Locate and identify every blood parasite.
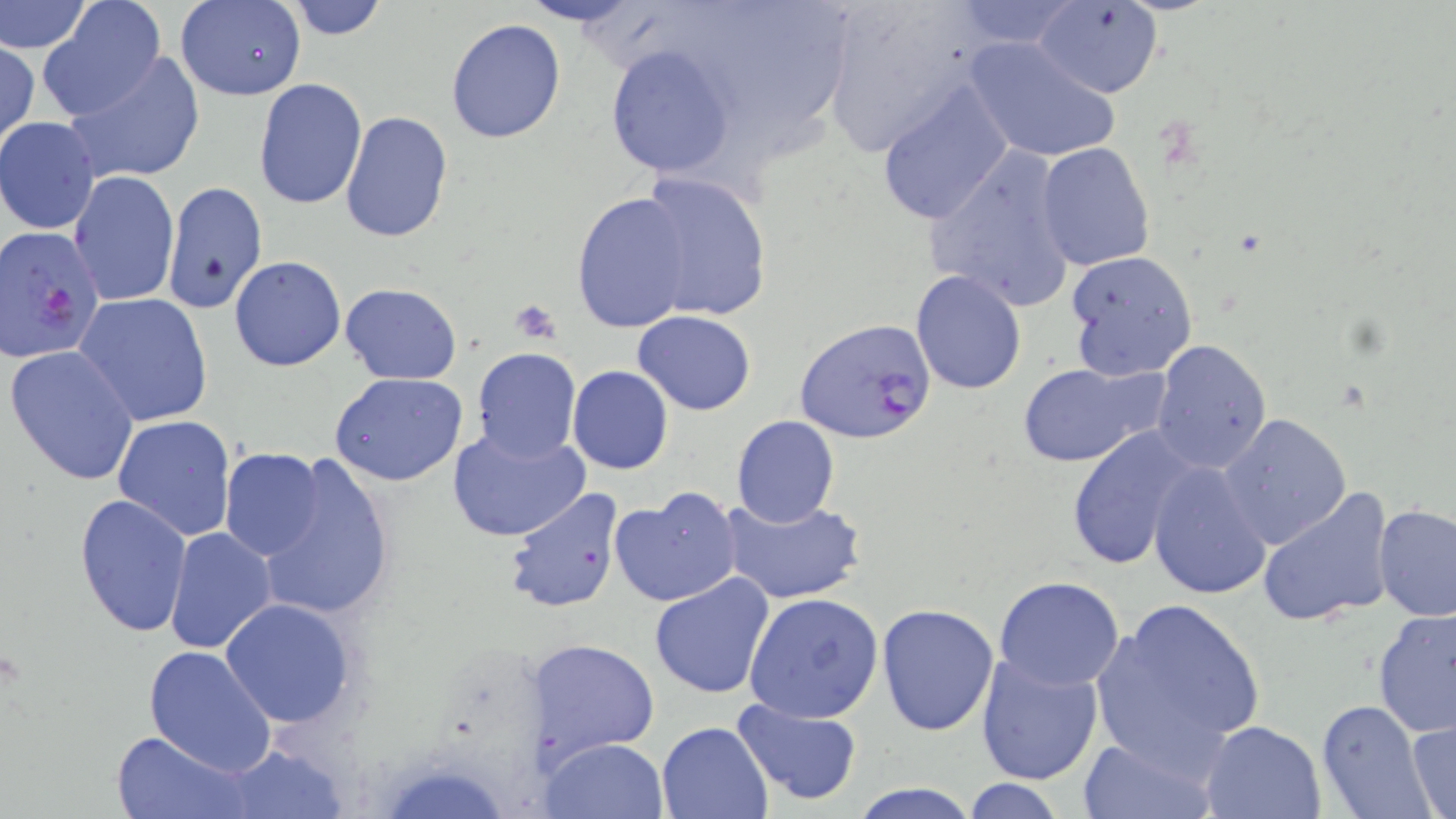
Approximate bounding boxes as named x1/y1/x2/y2 corners in pixels.
Plasmodium falciparum-infected red blood cells: (x1=1, y1=225, x2=105, y2=363), (x1=795, y1=319, x2=939, y2=446).
No Plasmodium ovale, Plasmodium malariae, Plasmodium vivax, Babesia divergens, or Trypanosoma brucei observed.

Platelet locations: (x1=507, y1=298, x2=561, y2=343). Uninfected red blood cell locations: (x1=0, y1=0, x2=90, y2=54), (x1=174, y1=0, x2=307, y2=102), (x1=282, y1=0, x2=391, y2=41), (x1=819, y1=0, x2=981, y2=158), (x1=1032, y1=2, x2=1164, y2=99), (x1=40, y1=3, x2=168, y2=119), (x1=444, y1=18, x2=566, y2=143), (x1=965, y1=37, x2=1124, y2=166), (x1=1, y1=39, x2=39, y2=151), (x1=605, y1=43, x2=736, y2=180), (x1=61, y1=50, x2=206, y2=187), (x1=873, y1=74, x2=1015, y2=225), (x1=252, y1=78, x2=368, y2=211), (x1=339, y1=111, x2=453, y2=244), (x1=1, y1=116, x2=101, y2=234), (x1=1036, y1=142, x2=1156, y2=272), (x1=926, y1=145, x2=1077, y2=314), (x1=68, y1=170, x2=179, y2=307), (x1=637, y1=170, x2=772, y2=322), (x1=571, y1=191, x2=695, y2=334), (x1=1064, y1=250, x2=1199, y2=381), (x1=228, y1=256, x2=346, y2=373), (x1=910, y1=271, x2=1027, y2=395), (x1=340, y1=283, x2=465, y2=383), (x1=75, y1=294, x2=215, y2=429), (x1=633, y1=311, x2=758, y2=415), (x1=1149, y1=340, x2=1272, y2=472), (x1=5, y1=346, x2=139, y2=487), (x1=470, y1=348, x2=582, y2=463), (x1=1018, y1=358, x2=1172, y2=467), (x1=568, y1=366, x2=672, y2=475), (x1=330, y1=372, x2=468, y2=487), (x1=1219, y1=413, x2=1352, y2=549), (x1=112, y1=414, x2=237, y2=542), (x1=731, y1=415, x2=840, y2=527), (x1=1064, y1=421, x2=1202, y2=571), (x1=446, y1=425, x2=590, y2=544), (x1=221, y1=450, x2=329, y2=560), (x1=250, y1=450, x2=396, y2=622), (x1=1147, y1=459, x2=1271, y2=600), (x1=1258, y1=484, x2=1396, y2=628), (x1=502, y1=485, x2=626, y2=616), (x1=610, y1=486, x2=744, y2=607), (x1=74, y1=492, x2=193, y2=637), (x1=718, y1=493, x2=866, y2=605), (x1=1373, y1=503, x2=1456, y2=623), (x1=163, y1=526, x2=277, y2=655), (x1=648, y1=572, x2=777, y2=700), (x1=993, y1=575, x2=1126, y2=690), (x1=743, y1=592, x2=884, y2=723), (x1=219, y1=599, x2=355, y2=727), (x1=1089, y1=599, x2=1265, y2=769), (x1=877, y1=604, x2=1000, y2=736), (x1=1372, y1=609, x2=1456, y2=738), (x1=1349, y1=623, x2=1449, y2=809), (x1=532, y1=638, x2=661, y2=763), (x1=143, y1=644, x2=277, y2=774), (x1=974, y1=652, x2=1106, y2=787), (x1=730, y1=699, x2=864, y2=807), (x1=1316, y1=699, x2=1436, y2=819), (x1=1201, y1=719, x2=1328, y2=818), (x1=1407, y1=719, x2=1455, y2=817), (x1=658, y1=720, x2=773, y2=818), (x1=112, y1=732, x2=247, y2=818), (x1=1078, y1=734, x2=1216, y2=818), (x1=540, y1=737, x2=670, y2=819), (x1=217, y1=744, x2=349, y2=817), (x1=958, y1=778, x2=1069, y2=818), (x1=844, y1=780, x2=986, y2=818). Slide-level diagnosis: Plasmodium falciparum. Captured at 1000x magnification. Image is 1456×819 pixels. Thin blood film. Optical microscopy. One field of a larger specimen. May-Grünwald-Giemsa-stained preparation.